Classify this cell by malaria status.
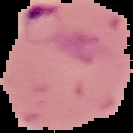
It is parasitized.

Summary:
  - Image size: 133×133 pixels
  - Image type: segmented cell region on a black background
  - Preparation: thin blood smear